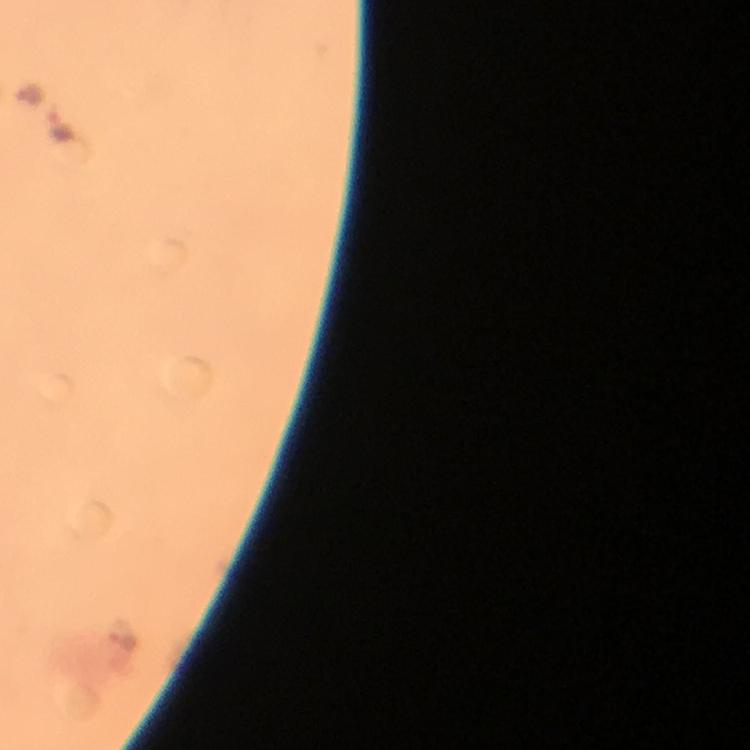

Approximate centers as {x, y} in pixels.
Summary:
  - Malaria parasite locations: {63, 128}, {123, 635}
  - Image size: 750×750 pixels
  - Capture: smartphone photograph through a microscope
  - Magnification: 100x
  - Cropped from: one field of view
  - Immersion oil: applied
  - Context: from a diagnostic examination for malaria
  - Stain: Giemsa
  - Preparation: thick blood film